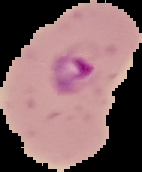 Cell region segmented out of the field of view; the surrounding area is masked to black. Malaria status: parasitized. From a thin blood film. Image is 142×172 pixels.